Name the parasite shown.
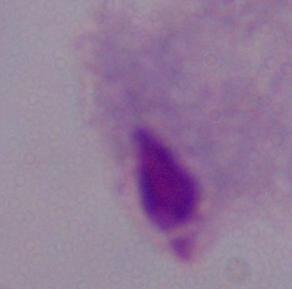
A trichomonad.

1000x magnification. Micrograph.